Classify this cell by malaria status.
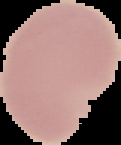
It is uninfected.

Summary:
  - Preparation: thin blood smear
  - Image type: segmented cell region on a black background
  - Image size: 121×145 pixels